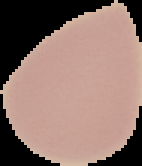

Summary:
  - Preparation: thin blood film
  - Image size: 142×166 pixels
  - Image type: segmented cell region on a black background
  - Malaria status: uninfected